Give the extent of all Trypanosoma brucei.
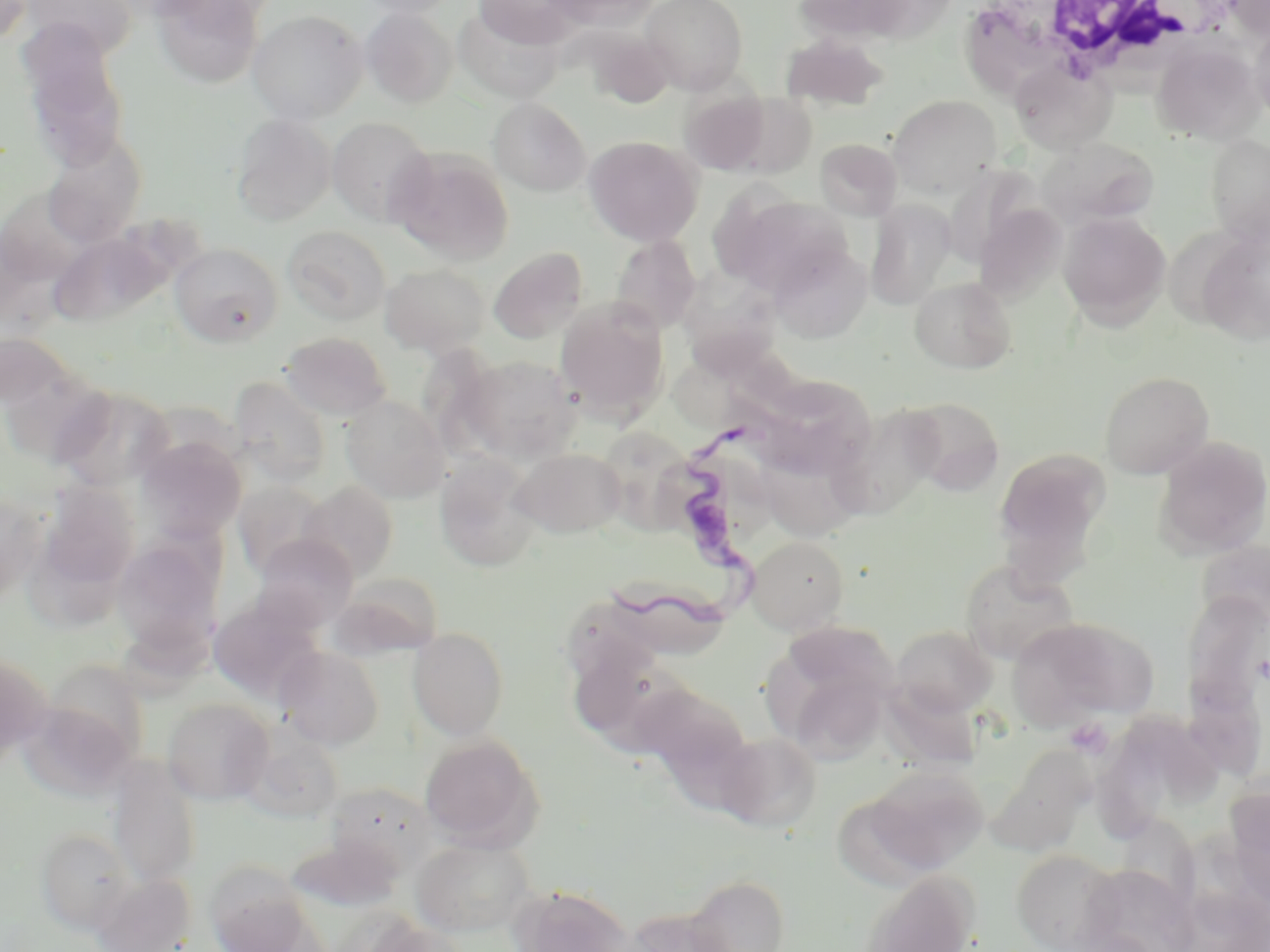
Approximate bounding boxes as [x1, y1, x2, y2] in pixels.
Trypanosoma brucei: [609, 418, 762, 646].

Uninfected red blood cell locations: [0, 0, 33, 43], [358, 0, 459, 18], [472, 0, 581, 49], [549, 0, 662, 30], [642, 0, 748, 93], [794, 0, 925, 43], [1226, 0, 1270, 38], [21, 1, 138, 58], [153, 1, 263, 88], [453, 6, 566, 104], [360, 7, 458, 107], [247, 9, 368, 123], [1249, 22, 1270, 123], [781, 34, 889, 110], [1153, 42, 1262, 144], [22, 44, 130, 173], [1010, 61, 1117, 154], [679, 90, 774, 175], [727, 94, 817, 176], [888, 94, 1003, 198], [488, 98, 591, 196], [231, 114, 335, 225], [327, 117, 435, 226], [40, 130, 147, 247], [1206, 133, 1269, 241], [584, 135, 704, 246], [1037, 136, 1159, 230], [814, 137, 902, 220], [388, 148, 514, 265], [943, 166, 1037, 269], [722, 194, 849, 299], [866, 200, 956, 309], [973, 202, 1066, 302], [1058, 211, 1171, 327], [282, 225, 391, 325], [1196, 227, 1270, 344], [48, 230, 169, 327], [610, 235, 702, 334], [768, 242, 872, 344], [169, 243, 283, 347], [488, 247, 588, 344], [379, 263, 491, 356], [681, 265, 786, 385], [909, 276, 1017, 374], [555, 300, 669, 421], [280, 331, 392, 421], [675, 351, 813, 435], [458, 354, 579, 463], [1099, 370, 1215, 478], [229, 376, 332, 486], [752, 385, 878, 481], [51, 386, 175, 491], [340, 395, 450, 502], [902, 396, 1005, 495], [838, 402, 942, 525], [1153, 435, 1270, 559], [137, 436, 246, 541], [993, 446, 1110, 573], [511, 448, 626, 537], [435, 454, 541, 571], [298, 481, 398, 582], [233, 482, 328, 579], [35, 483, 141, 597], [0, 492, 45, 601], [251, 534, 359, 632], [746, 534, 849, 634], [112, 537, 223, 657], [959, 558, 1078, 664], [232, 571, 345, 677], [1183, 587, 1268, 757], [209, 599, 323, 702], [1048, 619, 1160, 718], [1006, 620, 1125, 730], [890, 625, 996, 718], [408, 627, 509, 740], [568, 642, 693, 755], [276, 645, 384, 749], [0, 654, 49, 760], [43, 662, 150, 769], [779, 670, 890, 769], [622, 676, 752, 787], [161, 697, 273, 805], [16, 699, 136, 804], [239, 725, 344, 822], [714, 731, 822, 832], [418, 733, 543, 850], [1093, 743, 1173, 838], [986, 749, 1094, 857], [107, 761, 200, 889], [862, 765, 988, 874], [325, 781, 438, 878], [1224, 784, 1270, 907], [1115, 816, 1200, 911], [36, 828, 136, 933], [413, 836, 534, 936], [1011, 849, 1122, 951], [204, 861, 314, 951], [1079, 865, 1196, 951], [856, 871, 978, 952], [92, 873, 195, 952], [685, 874, 790, 952], [509, 884, 635, 952], [621, 906, 736, 951]. Platelet locations: [1065, 718, 1112, 758]. White blood cell locations: [996, 0, 1224, 84]. Slide-level diagnosis: Trypanosoma brucei. Optical microscopy. May-Grünwald-Giemsa stain. 1000x magnification. Image is 1270×952 pixels. Thin blood smear. One field of a larger specimen.